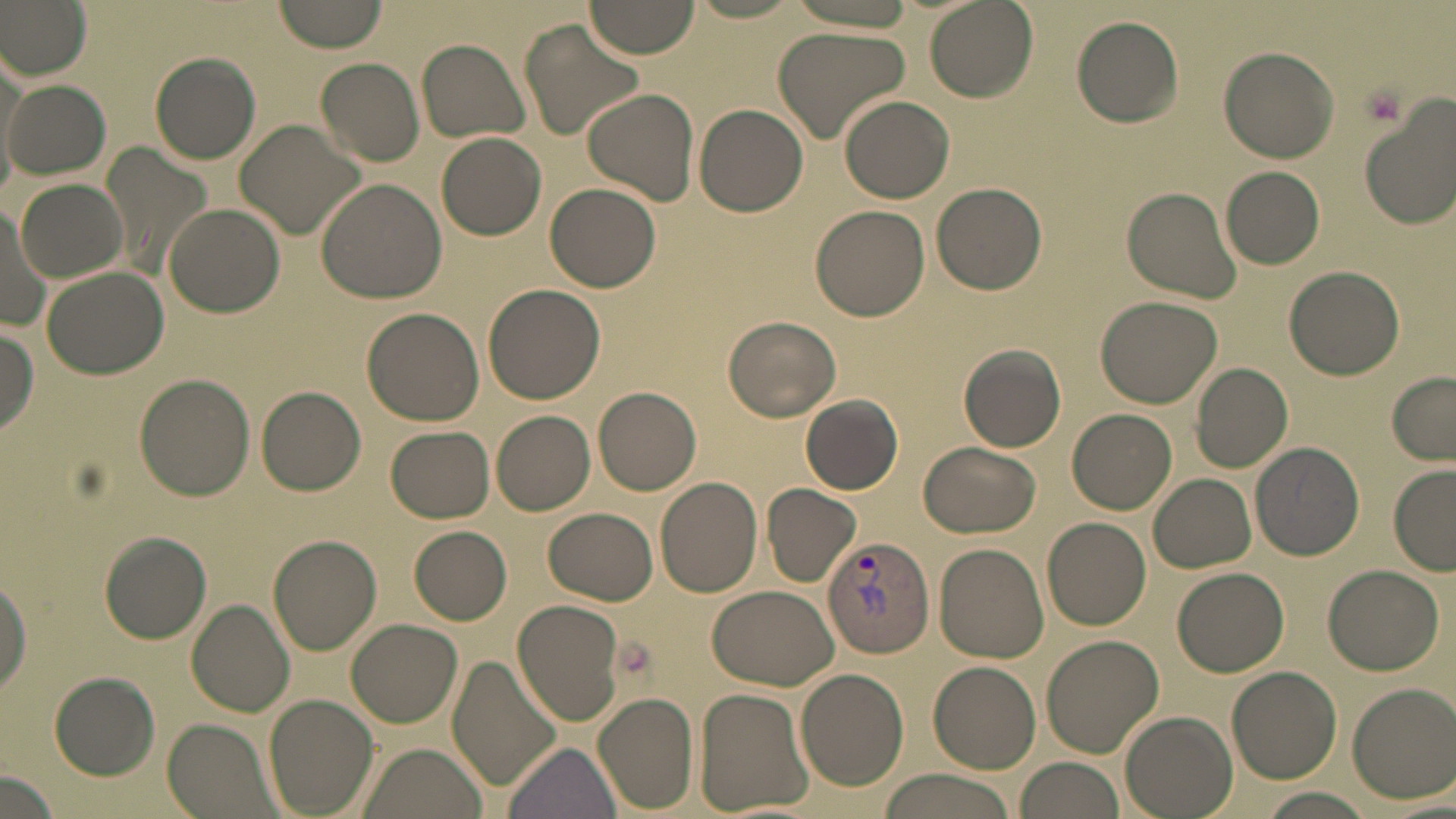
{
  "slide_level_diagnosis": "Plasmodium vivax",
  "magnification": "1000x",
  "field_of_view": "single",
  "uninfected_red_blood_cell_locations": "approximate bounding boxes as (x1, y1, x2, y2) in pixels: (0, 0, 91, 80), (271, 0, 390, 54), (584, 0, 700, 60), (685, 0, 808, 23), (780, 0, 922, 36), (924, 0, 1038, 103), (1071, 16, 1184, 127), (518, 17, 644, 142), (772, 25, 912, 143), (417, 38, 532, 143), (1218, 47, 1339, 163), (149, 52, 261, 164), (315, 57, 425, 167), (4, 79, 110, 179), (583, 88, 700, 203), (839, 95, 955, 203), (1359, 102, 1456, 230), (694, 103, 808, 217), (236, 120, 366, 240), (436, 131, 547, 241), (103, 141, 211, 275), (1221, 166, 1325, 269), (315, 178, 447, 303), (16, 179, 124, 281), (545, 182, 662, 292), (930, 182, 1047, 294), (1121, 185, 1242, 303), (164, 201, 287, 317), (0, 203, 52, 334), (809, 204, 930, 321), (1285, 265, 1403, 380), (42, 266, 169, 379), (483, 283, 604, 404), (1095, 295, 1221, 407), (362, 307, 485, 425), (722, 316, 842, 422), (0, 329, 39, 437), (957, 344, 1066, 453), (1189, 362, 1293, 472), (1386, 371, 1456, 466), (134, 373, 256, 500), (256, 386, 367, 496), (593, 387, 702, 496), (800, 395, 904, 496), (1067, 409, 1176, 514), (492, 411, 595, 514), (384, 425, 495, 523), (919, 440, 1041, 538), (1249, 442, 1366, 559), (1389, 465, 1456, 575), (1148, 475, 1257, 573), (655, 477, 762, 597), (762, 484, 862, 587), (543, 508, 656, 604), (1042, 516, 1152, 630), (408, 526, 511, 624), (97, 531, 212, 645), (268, 533, 382, 656), (933, 542, 1047, 661), (1321, 563, 1444, 675), (1173, 566, 1290, 677), (0, 572, 32, 699), (707, 583, 839, 691), (188, 598, 296, 717), (512, 599, 624, 725), (345, 619, 462, 728), (1039, 635, 1164, 757), (445, 656, 561, 792), (928, 661, 1041, 772), (1227, 666, 1342, 783), (796, 668, 908, 791), (48, 672, 159, 780), (1347, 684, 1456, 803), (695, 687, 813, 813), (592, 690, 700, 813), (261, 694, 379, 817), (1119, 710, 1238, 818), (164, 719, 282, 819), (501, 740, 621, 819), (358, 744, 487, 819), (1015, 757, 1123, 819), (0, 768, 59, 819), (876, 770, 1024, 819), (1250, 788, 1376, 819)",
  "modality": "light microscopy",
  "platelet_locations": "approximate bounding boxes as (x1, y1, x2, y2) in pixels: (1360, 81, 1408, 126)",
  "stain": "May-Grünwald-Giemsa",
  "plasmodium_vivax_infected_red_blood_cell_locations": "approximate bounding boxes as (x1, y1, x2, y2) in pixels: (822, 535, 935, 658)",
  "image_size": "1456×819 pixels",
  "preparation": "thin blood film"
}